Identify the blood parasite species.
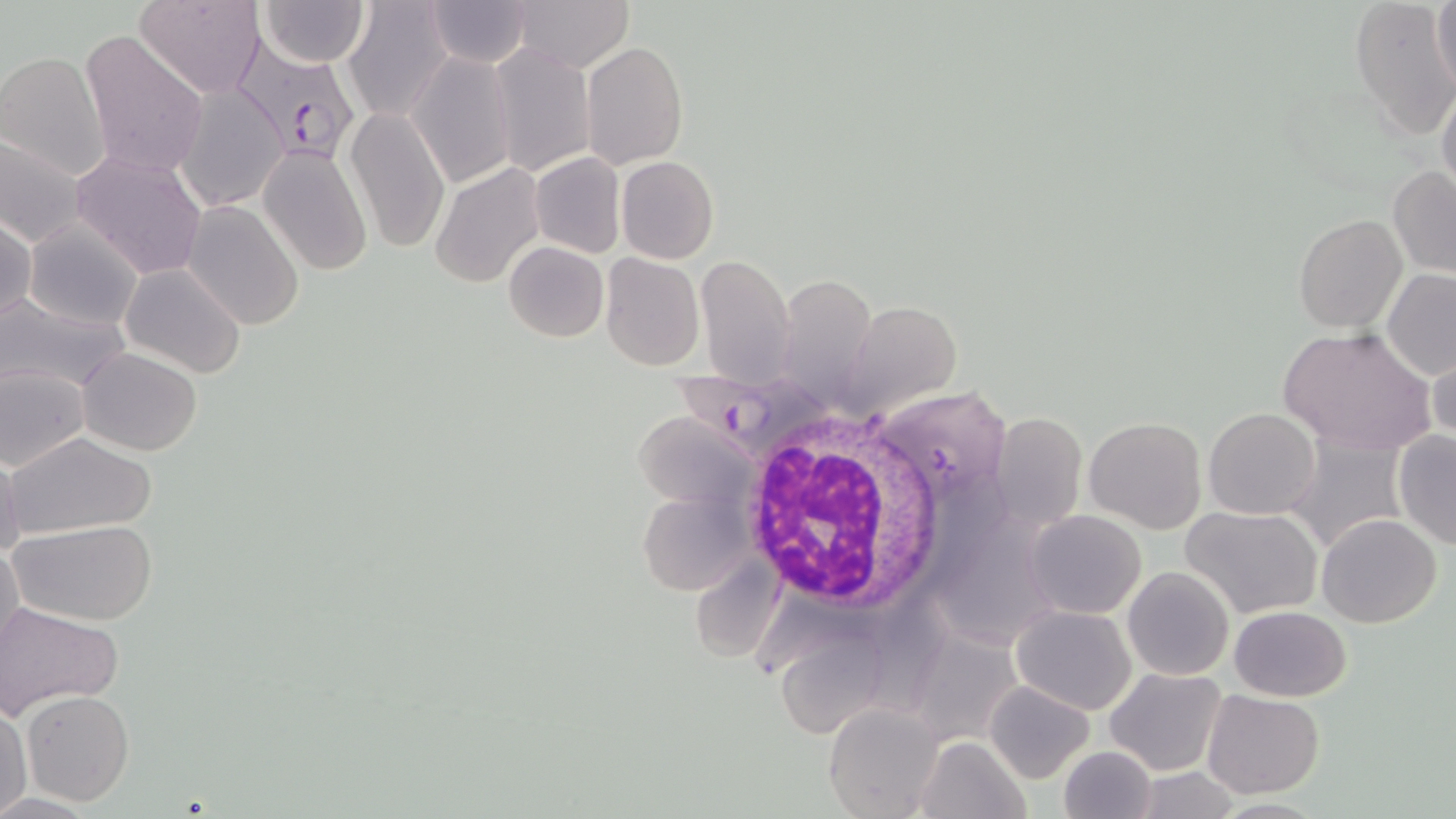

Plasmodium falciparum.

Summary:
  - Coordinate format: approximate bounding boxes as (x1,y1)-(x2,y2) corner pairs in pixels
  - Plasmodium falciparum-infected red blood cell locations: (233,44)-(362,162), (669,367)-(839,458)
  - Uninfected red blood cell locations: (136,0)-(262,99), (257,0)-(370,68), (1429,0)-(1456,99), (428,1)-(533,68), (513,1)-(631,72), (343,2)-(453,123), (1349,3)-(1455,143), (79,30)-(211,181), (581,41)-(688,169), (488,43)-(596,176), (0,52)-(111,182), (408,53)-(517,189), (174,84)-(287,210), (1436,87)-(1456,201), (343,106)-(450,255), (0,131)-(87,249), (258,145)-(374,279), (72,150)-(208,280), (529,151)-(626,258), (616,155)-(718,264), (430,164)-(545,288), (1387,165)-(1456,277), (183,200)-(306,332), (1294,213)-(1407,334), (0,214)-(36,326), (23,218)-(144,332), (504,241)-(608,342), (600,253)-(704,371), (694,254)-(796,385), (120,264)-(247,379), (786,267)-(879,401), (1381,269)-(1456,380), (0,296)-(129,396), (840,301)-(961,418), (1277,328)-(1435,454), (1427,345)-(1455,451), (76,347)-(203,457), (0,363)-(90,470), (1203,407)-(1321,520), (635,410)-(760,516), (990,412)-(1087,538), (1084,418)-(1206,535), (4,430)-(157,544), (1392,431)-(1456,549), (1287,432)-(1410,558), (0,451)-(23,562), (640,488)-(750,595), (946,499)-(1050,657), (1180,506)-(1323,619), (1026,509)-(1147,618), (1317,513)-(1442,627), (10,518)-(158,626), (0,539)-(24,660), (690,555)-(782,664), (1122,567)-(1233,680), (875,593)-(963,721), (2,603)-(125,715), (1011,605)-(1136,715), (1229,605)-(1351,702), (770,625)-(905,752), (909,629)-(1026,744), (1105,667)-(1227,776), (986,681)-(1095,784), (1203,688)-(1324,798), (22,690)-(134,807), (825,701)-(945,818), (0,705)-(32,814), (915,735)-(1029,819), (1058,744)-(1158,819)
  - White blood cell locations: (730,411)-(949,612)
  - Stain: May-Grünwald-Giemsa
  - Field of view: single
  - Preparation: thin blood smear
  - Image size: 1456×819 pixels
  - Magnification: 1000x
  - Modality: optical microscopy